Describe the morphology of the red blood cells.
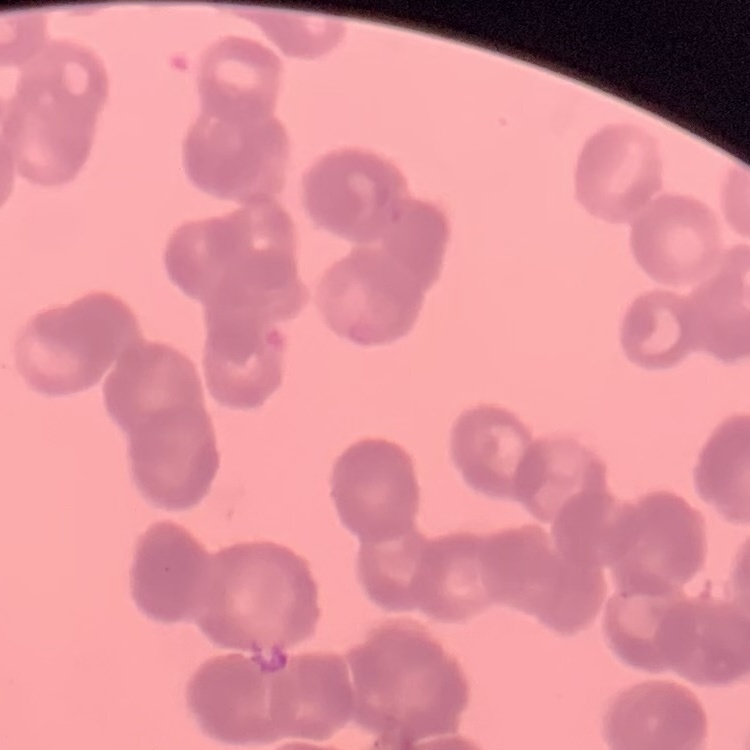
Rouleaux formation.

Summary:
  - Stain: Field's or Giemsa
  - Preparation: thin peripheral smear
  - Image type: one tile cut from a larger photomicrograph